Assess the morphology of the erythrocytes.
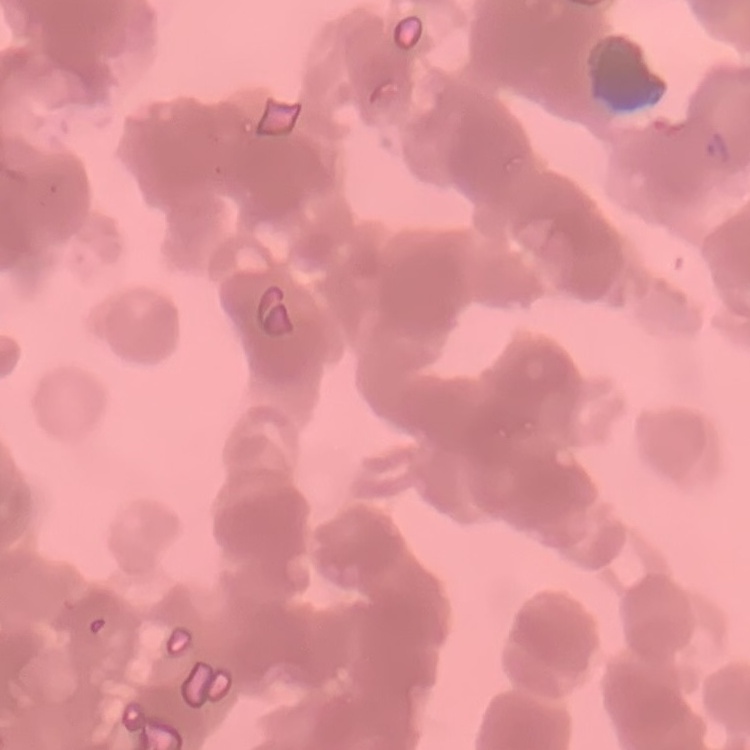

Rouleaux formation.

Summary:
  - Stain: Field's or Giemsa
  - Image type: square crop of a larger photomicrograph
  - Preparation: thin peripheral smear